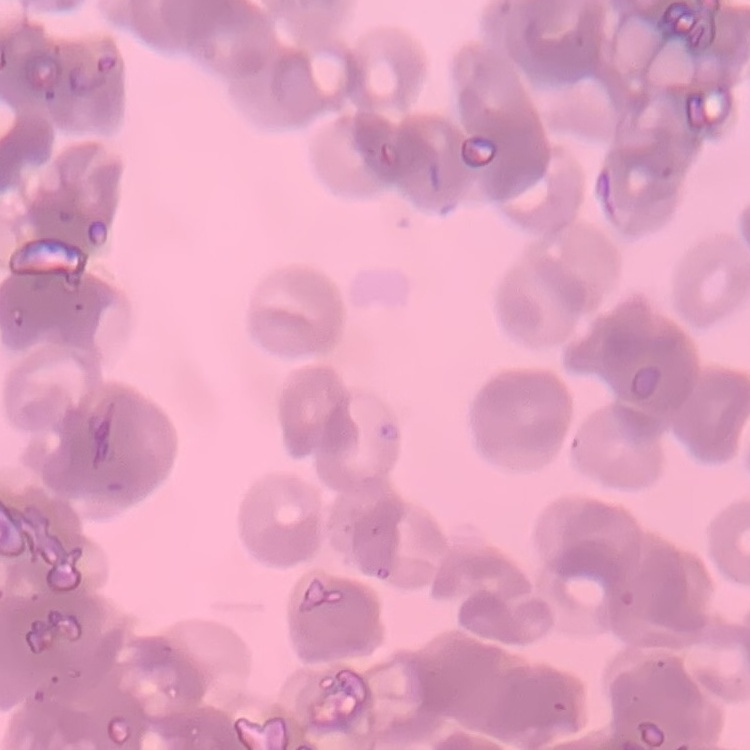
{
  "red_blood_cell_morphology": "rouleaux formation",
  "preparation": "thin blood film",
  "image_type": "one tile cut from a larger photomicrograph",
  "stain": "Field's or Giemsa"
}